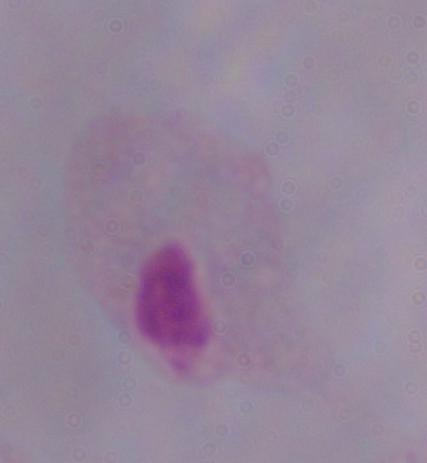
A trichomonad is shown. Micrograph. Captured at 1000x magnification.